Report the malaria status of this cell.
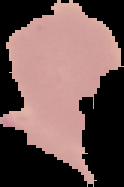

Uninfected.

{
  "preparation": "thin blood smear",
  "image_size": "124×187 pixels",
  "image_type": "segmented cell region with the area outside set to black"
}